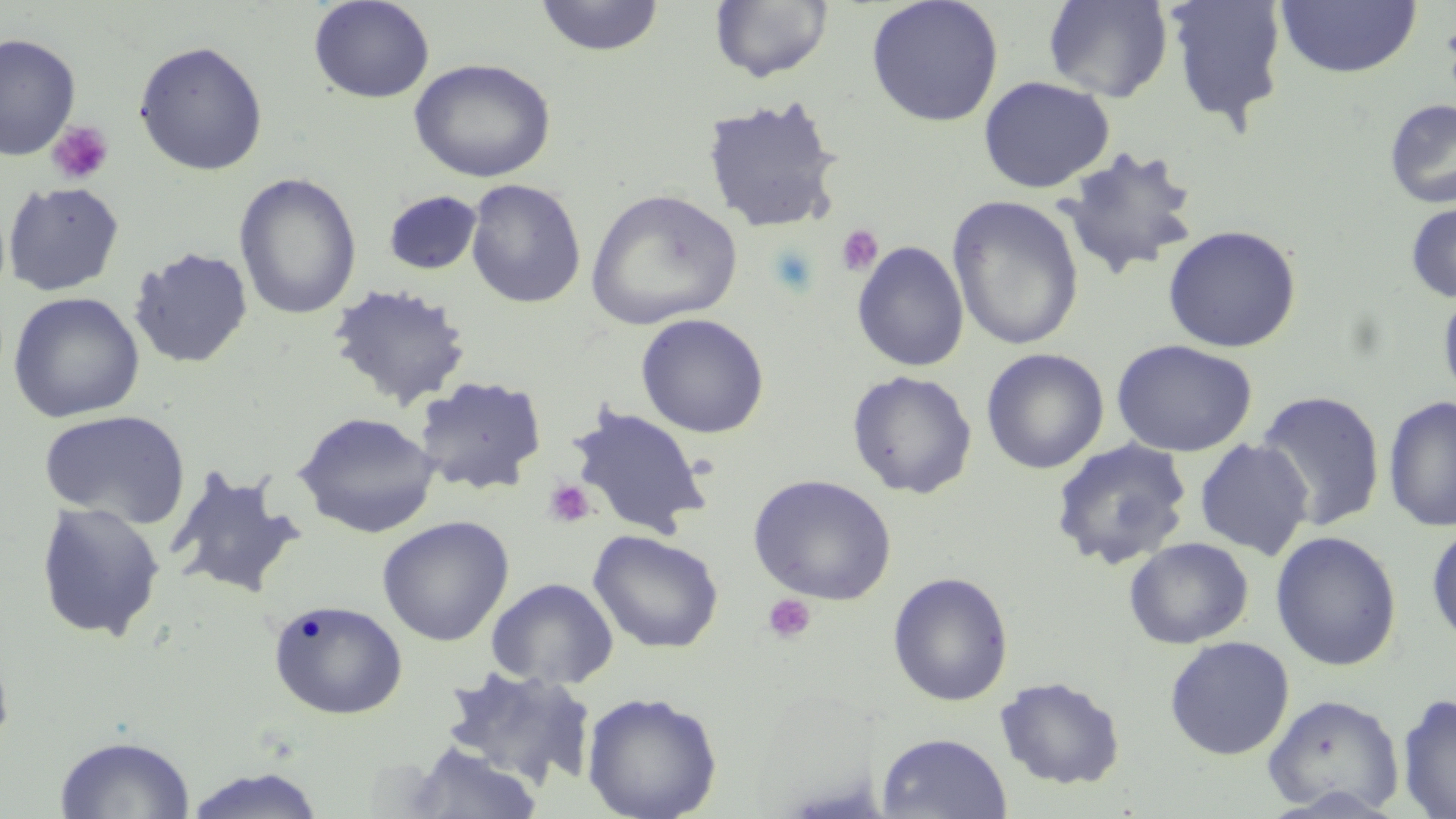

Summary:
  - Coordinate format: approximate bounding boxes as (x1,y1)-(x2,y2) corner pairs in pixels
  - Platelet locations: (46,120)-(114,186), (836,224)-(883,277), (543,479)-(596,527), (762,593)-(816,644)
  - Uninfected red blood cell locations: (308,0)-(435,104), (534,0)-(664,57), (866,0)-(1004,127), (1042,0)-(1173,102), (1164,0)-(1289,131), (709,1)-(834,83), (1275,1)-(1422,79), (0,34)-(81,161), (133,40)-(268,175), (408,58)-(557,183), (978,75)-(1114,193), (700,95)-(846,233), (1383,98)-(1456,209), (1057,145)-(1201,280), (233,172)-(362,320), (464,179)-(586,308), (3,180)-(125,296), (585,188)-(743,330), (383,190)-(483,275), (947,195)-(1085,351), (1405,199)-(1456,304), (1162,224)-(1302,353), (851,240)-(970,372), (129,246)-(254,370), (326,281)-(474,411), (1437,282)-(1456,408), (7,291)-(145,423), (635,313)-(770,438), (1111,339)-(1257,457), (981,347)-(1109,474), (847,369)-(978,498), (414,375)-(548,495), (1254,390)-(1386,531), (1383,395)-(1456,532), (565,404)-(713,539), (38,408)-(191,529), (293,411)-(441,539), (1050,438)-(1193,570), (1194,438)-(1314,559), (166,467)-(305,600), (747,475)-(897,606), (34,501)-(166,642), (377,515)-(514,646), (1426,522)-(1456,646), (588,529)-(724,654), (1270,530)-(1402,671), (1124,537)-(1253,649), (887,571)-(1014,707), (486,577)-(619,689), (267,598)-(408,720), (1164,636)-(1295,760), (0,637)-(16,758), (437,666)-(597,790), (994,676)-(1126,790), (581,691)-(723,819), (1262,693)-(1404,817), (1397,693)-(1456,818), (876,732)-(1012,818), (54,734)-(197,818), (403,742)-(543,818), (181,766)-(329,818)
  - Slide-level diagnosis: negative for blood parasites
  - Stain: May-Grünwald-Giemsa
  - Preparation: thin blood film
  - Magnification: 1000x
  - Image size: 1456×819 pixels
  - Modality: light microscopy
  - Field of view: one of a larger specimen